Locate every blood parasite and identify its species.
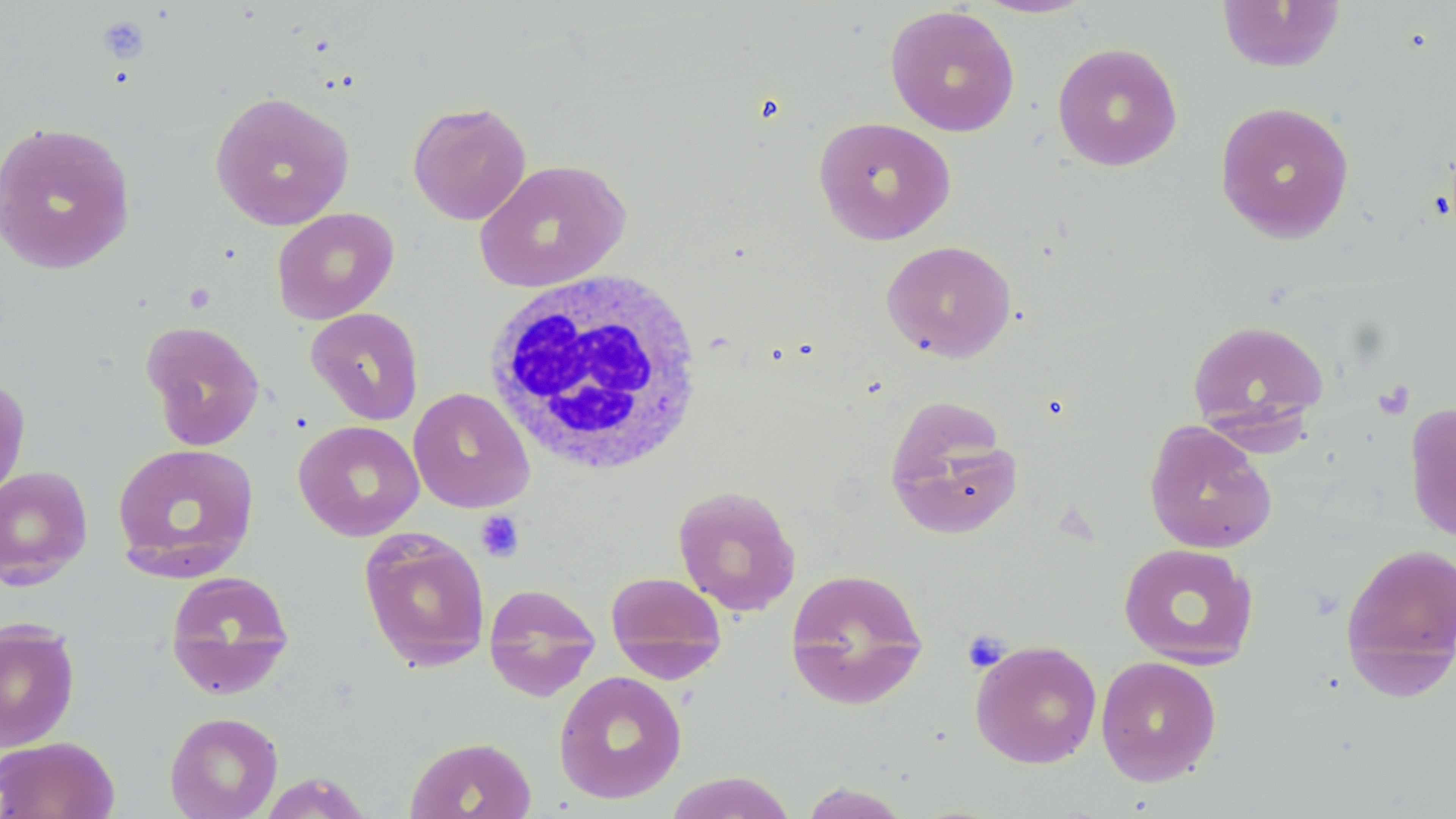
No blood parasites seen.

Summary:
  - Coordinate format: approximate bounding boxes as [x1, y1, x2, y2] in pixels
  - White blood cell locations: [480, 270, 708, 477]
  - Uninfected red blood cell locations: [973, 0, 1094, 18], [1215, 0, 1347, 74], [884, 4, 1020, 137], [1052, 42, 1183, 171], [210, 91, 354, 231], [407, 100, 531, 225], [1214, 101, 1355, 243], [813, 116, 956, 245], [0, 120, 137, 275], [474, 158, 631, 294], [271, 207, 399, 324], [881, 240, 1017, 363], [305, 307, 424, 425], [1187, 318, 1330, 442], [141, 319, 266, 451], [0, 374, 31, 503], [408, 387, 534, 512], [884, 398, 1023, 539], [1404, 402, 1456, 544], [293, 420, 425, 541], [1143, 420, 1277, 554], [111, 442, 260, 581], [0, 465, 93, 589], [672, 484, 801, 616], [359, 529, 491, 672], [1339, 541, 1456, 697], [1118, 542, 1259, 669], [785, 567, 929, 711], [165, 570, 295, 700], [605, 570, 727, 682], [484, 583, 601, 701], [0, 619, 81, 751], [970, 639, 1103, 768], [1095, 655, 1222, 785], [553, 670, 687, 804], [164, 711, 283, 818], [0, 735, 120, 819], [404, 736, 537, 819], [664, 771, 798, 818], [257, 772, 374, 817], [797, 782, 915, 818]
  - Platelet locations: [96, 16, 151, 64], [1372, 380, 1415, 421], [475, 511, 524, 562], [962, 629, 1011, 672]
  - Slide-level diagnosis: no evidence of blood parasites
  - Modality: light microscopy
  - Preparation: thin blood film
  - Stain: May-Grünwald-Giemsa
  - Image size: 1456×819 pixels
  - Field of view: single
  - Magnification: 1000x